Describe the morphology of the red blood cells.
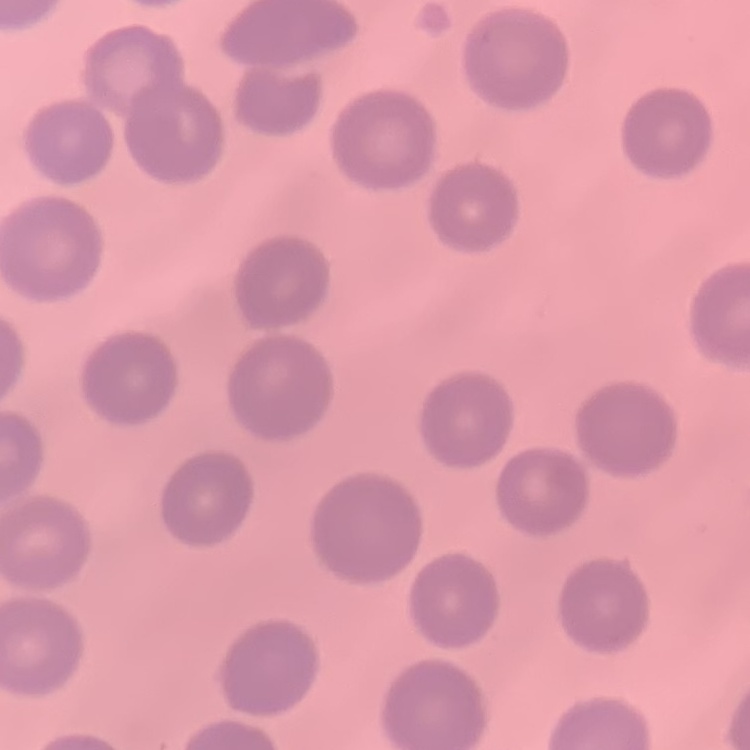

They show no rouleaux formation.

preparation = thin blood smear
stain = Field's or Giemsa
image type = square crop of a larger photomicrograph